Report the malaria status of this cell.
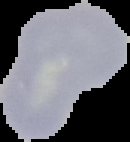

It is uninfected.

Summary:
  - Image type: segmented cell region on a black background
  - Image size: 130×142 pixels
  - Preparation: thin blood film